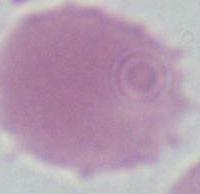
Captured at 1000x magnification. A red blood cell is shown. Photomicrograph.